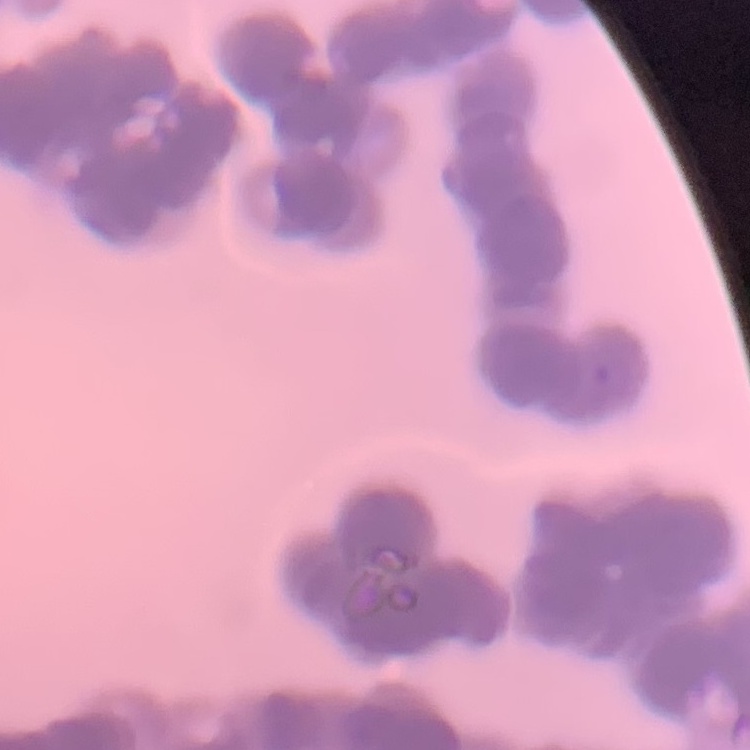 The red blood cells show rouleaux formation. One tile cut from a larger photomicrograph. Thin peripheral smear. Field's or Giemsa stain.